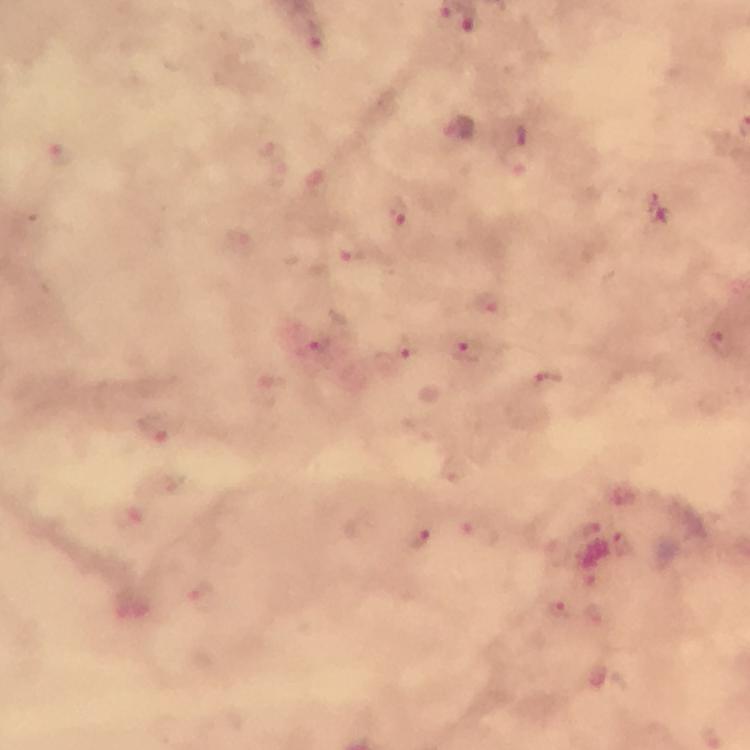

preparation = thick smear
immersion oil = used
magnification = 100x
capture = smartphone photograph through a microscope
Plasmodium parasite locations = approximate centers as (x, y) in pixels: (470, 20), (316, 36), (61, 153), (516, 158), (398, 213), (355, 255), (488, 303), (318, 342), (719, 343), (405, 349), (468, 351), (548, 380), (152, 427), (478, 536), (419, 541), (556, 610), (591, 614)
context = from a diagnostic examination for malaria
cropped from = one field of view
stain = Giemsa
image size = 750×750 pixels